Report the malaria status of this cell.
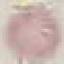
It is uninfected.

Summary:
  - Image type: cell patch, automatically extracted from a larger field of view and resized to 64 × 64 pixels
  - Capture: smartphone camera at the microscope eyepiece
  - Stain: Giemsa
  - Preparation: thin blood film